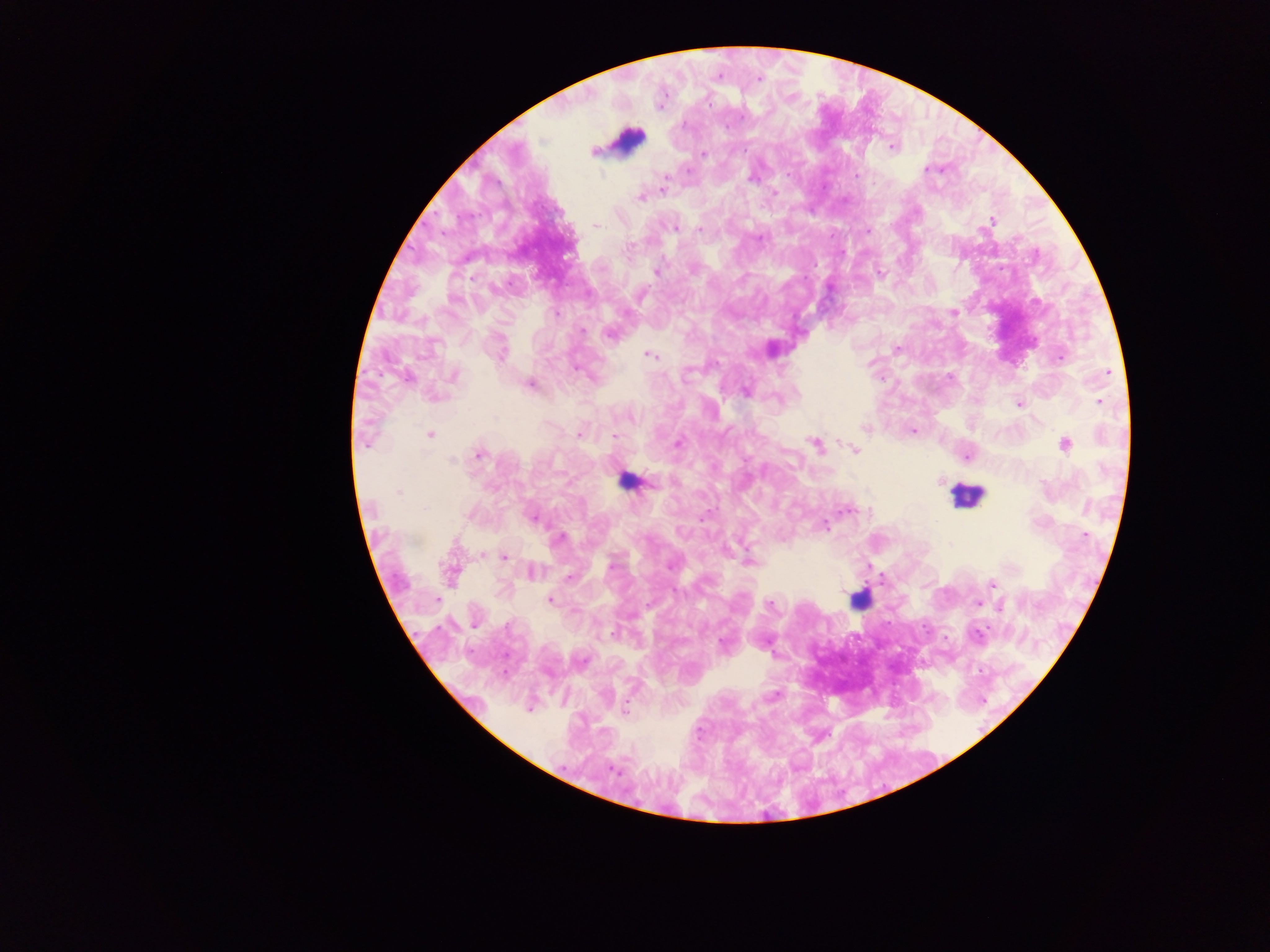

Approximate centers as {x, y} in pixels.
Summary:
  - Leukocyte locations: {628, 132}, {625, 481}, {967, 497}, {858, 603}
  - Plasmodium parasite locations: {759, 73}, {717, 77}, {758, 78}, {707, 98}, {791, 99}, {890, 146}, {592, 152}, {701, 153}, {924, 172}, {929, 172}, {750, 181}, {662, 189}, {776, 193}, {640, 196}, {919, 213}, {992, 220}, {674, 224}, {597, 226}, {699, 228}, {676, 230}, {655, 273}, {641, 296}, {556, 313}, {953, 313}, {582, 332}, {609, 334}, {896, 349}, {774, 351}, {647, 355}, {1060, 356}, {574, 369}, {1107, 371}, {455, 374}, {688, 374}, {531, 384}, {798, 390}, {745, 392}, {1100, 400}, {1020, 404}, {633, 418}, {865, 429}, {913, 432}, {432, 434}, {580, 434}, {615, 434}, {365, 442}, {678, 442}, {813, 443}, {1066, 445}, {854, 450}, {480, 454}, {968, 455}, {451, 462}, {939, 480}, {654, 483}, {536, 520}, {826, 526}, {683, 531}, {1083, 536}, {561, 538}, {948, 544}, {484, 553}, {504, 557}, {749, 560}, {531, 572}, {452, 574}, {570, 577}, {993, 583}, {437, 599}, {551, 599}, {977, 601}, {769, 603}, {1001, 607}, {614, 633}, {976, 636}, {722, 644}, {775, 694}, {622, 709}, {613, 766}
  - Field of view: single
  - Country: Ghana
  - Image size: 1270×952 pixels
  - Capture: mobile-phone photograph through a microscope
  - Preparation: thick blood smear